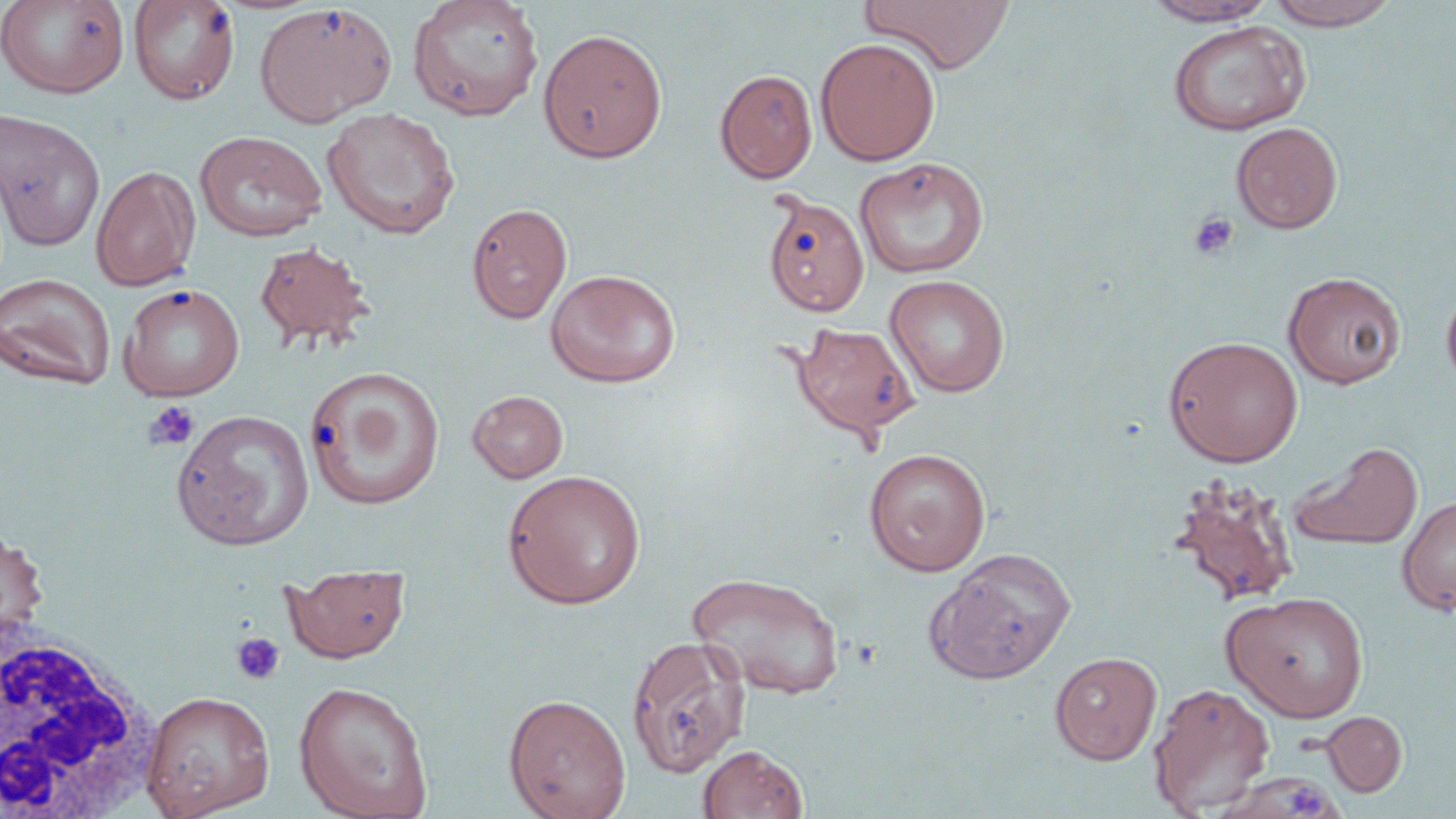
slide-level diagnosis = negative for blood parasites
stain = May-Grünwald-Giemsa
preparation = thin blood film
platelet locations = approximate bounding boxes as [x1, y1, x2, y2] in pixels: [1188, 212, 1239, 261], [144, 401, 200, 452], [230, 632, 286, 686], [1292, 777, 1331, 818]
field of view = single
magnification = 1000x
image size = 1456×819 pixels
white blood cell locations = approximate bounding boxes as [x1, y1, x2, y2] in pixels: [0, 619, 162, 819]
modality = light microscopy
uninfected red blood cell locations = approximate bounding boxes as [x1, y1, x2, y2] in pixels: [127, 0, 240, 106], [406, 0, 544, 122], [858, 0, 1016, 74], [1264, 0, 1403, 29], [0, 1, 130, 99], [1140, 1, 1279, 27], [254, 4, 396, 127], [1168, 20, 1311, 136], [537, 28, 668, 164], [815, 37, 940, 166], [715, 69, 817, 184], [322, 107, 460, 240], [0, 109, 106, 252], [1231, 122, 1343, 234], [194, 130, 327, 241], [854, 157, 989, 279], [90, 165, 201, 292], [762, 193, 869, 318], [466, 203, 572, 324], [253, 240, 375, 353], [545, 269, 681, 388], [1283, 272, 1406, 389], [0, 273, 116, 390], [885, 274, 1011, 397], [1440, 283, 1456, 396], [118, 284, 245, 401], [790, 321, 920, 442], [1164, 335, 1303, 467], [304, 365, 445, 510], [467, 390, 569, 484], [171, 409, 315, 551], [1290, 441, 1423, 553], [864, 447, 992, 576], [501, 469, 647, 609], [1166, 476, 1301, 608], [1397, 496, 1456, 613], [0, 525, 49, 657], [925, 547, 1076, 685], [282, 563, 410, 663], [687, 571, 845, 700], [1223, 590, 1369, 723], [627, 634, 751, 777], [1049, 651, 1162, 765], [293, 681, 433, 819], [1148, 682, 1275, 816], [141, 690, 276, 819], [503, 693, 631, 819], [1322, 711, 1408, 797], [697, 744, 808, 818], [1211, 772, 1342, 818]